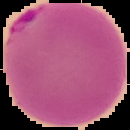
Result: malaria parasites identified. Image is 130×130 pixels. The area outside the segmented cell region is set to black. From a thin blood smear.